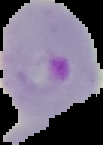
Summary:
  - Image type: segmented cell region on a black background
  - Malaria status: parasitized
  - Image size: 103×145 pixels
  - Preparation: thin blood smear